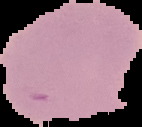

Image is 142×127 pixels. Malaria status: uninfected. Segmented cell region on a black background. From a thin blood smear.